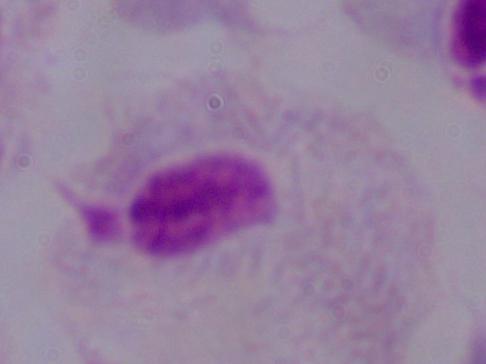

identification = trichomonad
modality = photomicrograph
magnification = 1000x